Name the parasite shown.
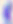
This is Toxoplasma gondii.

modality = micrograph
magnification = 400x